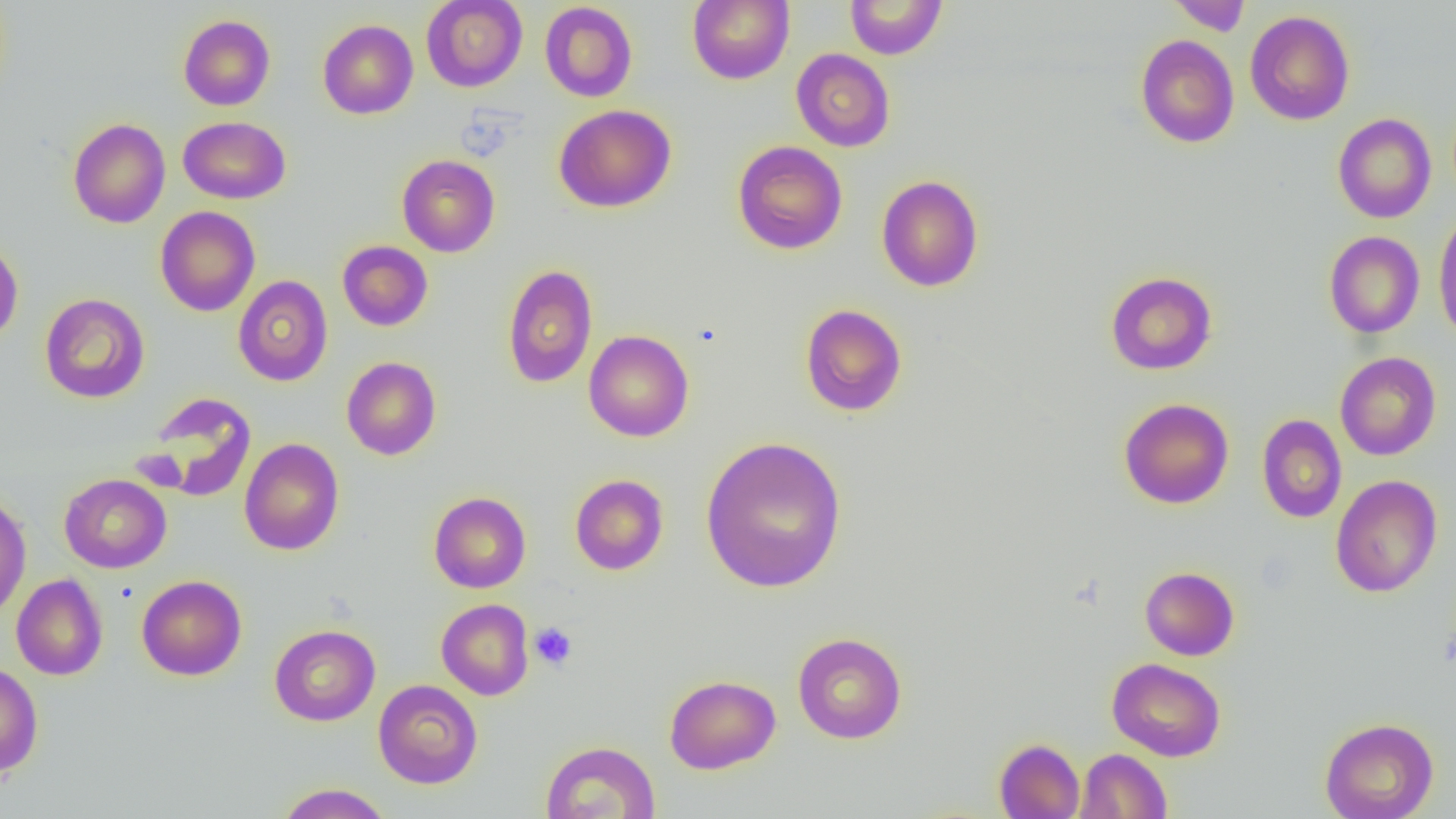

slide-level diagnosis = no evidence of blood parasites
magnification = 1000x
preparation = thin blood film
field of view = one of a larger specimen
modality = optical microscopy
uninfected red blood cell locations = approximate bounding boxes as [x1, y1, x2, y2] in pixels: [421, 0, 527, 91], [687, 0, 795, 85], [845, 0, 947, 59], [1167, 0, 1252, 35], [539, 2, 638, 102], [1244, 10, 1355, 126], [178, 14, 275, 110], [317, 19, 418, 119], [1135, 34, 1239, 148], [791, 48, 895, 152], [553, 104, 676, 213], [1333, 113, 1437, 223], [178, 116, 290, 204], [68, 118, 171, 228], [733, 141, 847, 255], [397, 154, 500, 257], [876, 175, 984, 292], [155, 206, 260, 316], [1433, 209, 1456, 345], [1324, 230, 1425, 338], [0, 239, 24, 345], [337, 240, 433, 331], [501, 264, 598, 388], [1105, 271, 1217, 375], [232, 275, 333, 386], [39, 293, 150, 403], [800, 304, 908, 416], [583, 330, 694, 442], [1334, 352, 1441, 460], [341, 357, 441, 460], [142, 392, 257, 502], [1118, 398, 1234, 509], [1257, 414, 1347, 523], [699, 436, 848, 593], [239, 438, 344, 556], [569, 473, 669, 575], [59, 474, 172, 573], [1331, 474, 1443, 598], [429, 491, 531, 593], [0, 493, 31, 619], [1140, 566, 1239, 660], [11, 574, 108, 680], [136, 575, 247, 681], [436, 598, 534, 700], [269, 624, 380, 726], [792, 632, 907, 744], [1107, 657, 1226, 762], [0, 663, 44, 776], [664, 674, 781, 774], [373, 679, 483, 789], [1319, 716, 1439, 819], [994, 738, 1084, 819], [540, 740, 660, 819], [1075, 748, 1172, 818], [275, 783, 393, 819]
image size = 1456×819 pixels
platelet locations = approximate bounding boxes as [x1, y1, x2, y2] in pixels: [529, 622, 578, 671]